Report the malaria status of this cell.
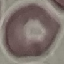

It is uninfected.

Giemsa-stained preparation. Photographed with a smartphone camera at the microscope eyepiece. Thin smear of blood. Automatically extracted cell patch, resized to 64 × 64 pixels.